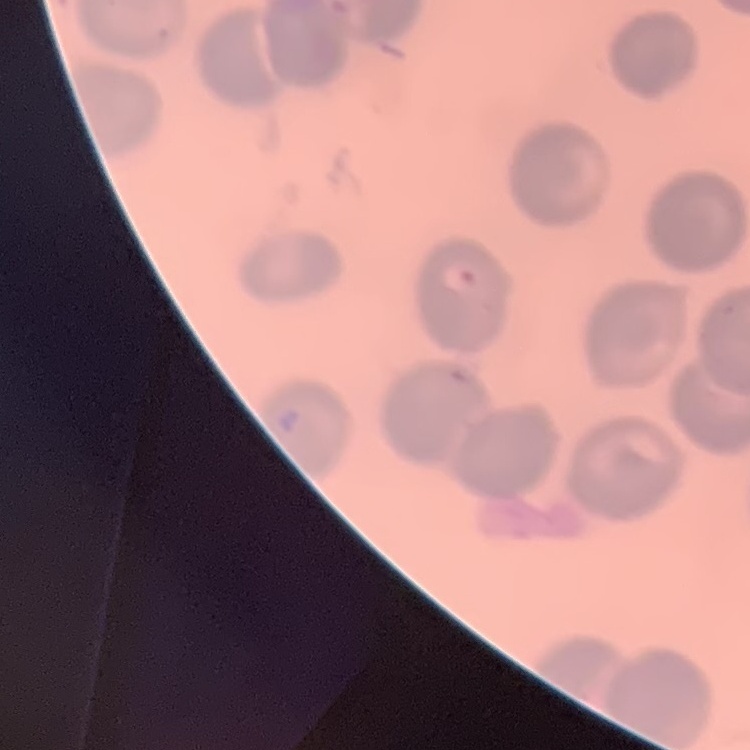
{
  "erythrocyte_morphology": "no rouleaux formation",
  "preparation": "thin peripheral smear",
  "image_type": "square crop of a larger photomicrograph",
  "stain": "Field's or Giemsa"
}